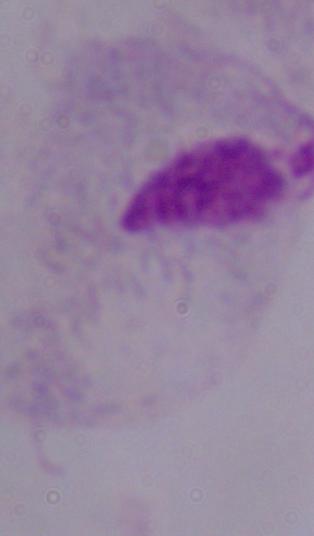 A trichomonad is seen. 1000x magnification. Photomicrograph.